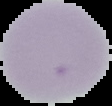

Summary:
  - Preparation: thin blood smear
  - Image type: segmented cell region on a black background
  - Image size: 112×106 pixels
  - Result: negative for Plasmodium parasites